Assess this cell for malaria.
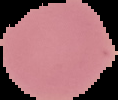
Uninfected.

Summary:
  - Image type: segmented cell region on a black background
  - Image size: 118×100 pixels
  - Preparation: thin blood smear